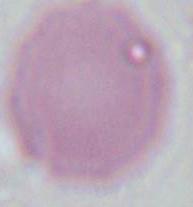

Summary:
  - Modality: micrograph
  - Magnification: 1000x
  - Identification: red blood cell